Locate and identify every blood parasite.
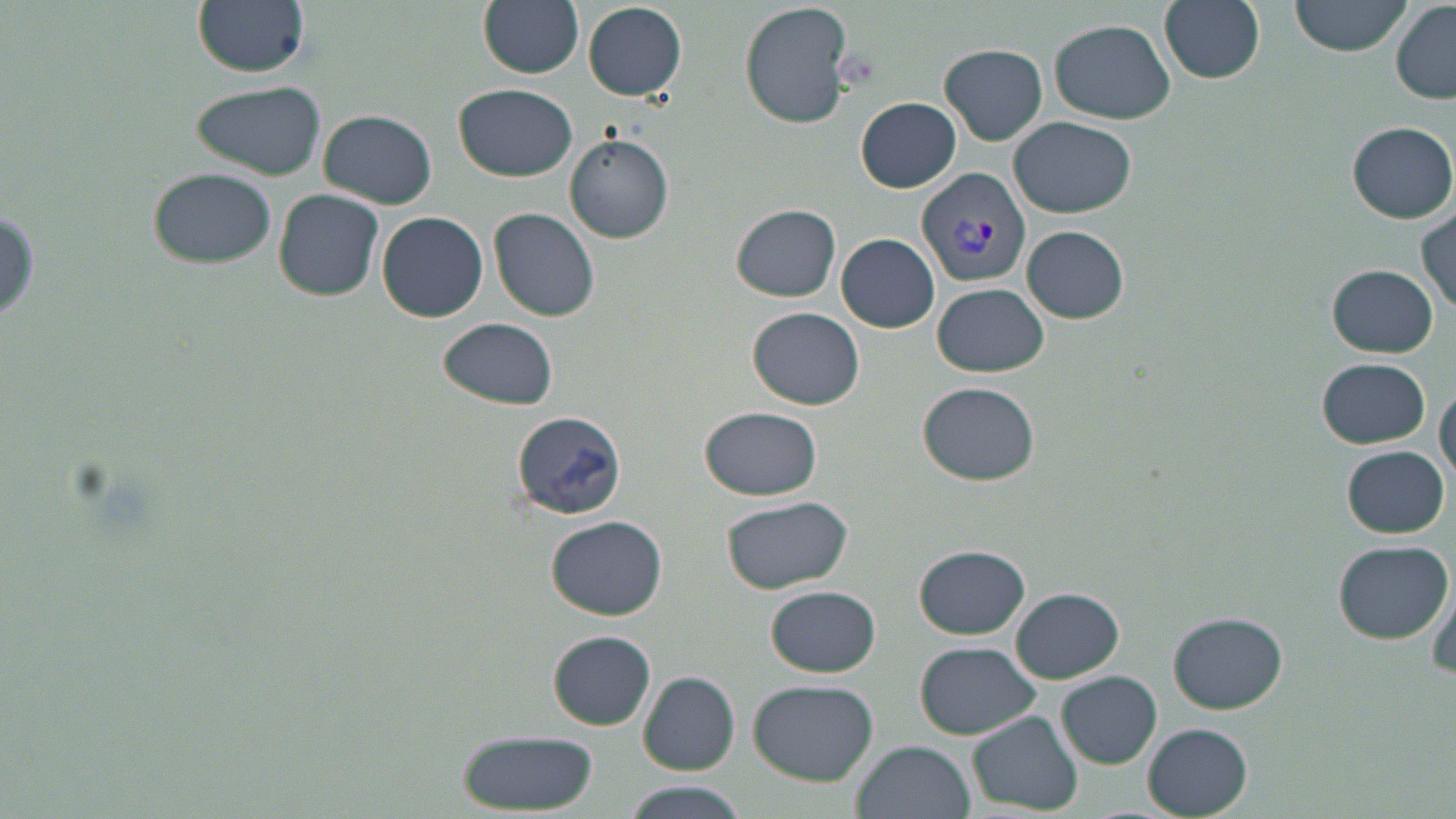

Approximate bounding boxes as (x1, y1, x2, y2) in pixels.
Plasmodium vivax-infected red blood cells: (916, 167, 1031, 290).
No Plasmodium falciparum, Plasmodium ovale, Plasmodium malariae, Babesia divergens, or Trypanosoma brucei observed.

Summary:
  - Uninfected red blood cell locations: (194, 0, 311, 77), (480, 0, 585, 77), (739, 0, 856, 131), (1158, 0, 1266, 85), (1290, 0, 1414, 56), (1392, 2, 1456, 103), (583, 3, 686, 100), (1049, 18, 1175, 123), (941, 43, 1049, 144), (189, 79, 327, 182), (454, 82, 578, 182), (857, 97, 960, 193), (317, 109, 437, 208), (1010, 115, 1136, 218), (1350, 121, 1455, 222), (564, 135, 674, 242), (149, 167, 276, 269), (274, 188, 384, 300), (731, 204, 841, 302), (1416, 205, 1455, 311), (489, 208, 601, 320), (377, 211, 488, 322), (1022, 226, 1128, 322), (837, 233, 939, 332), (1329, 265, 1439, 356), (932, 282, 1049, 378), (748, 307, 865, 410), (438, 316, 559, 411), (1316, 356, 1431, 448), (919, 381, 1038, 486), (1436, 382, 1456, 486), (700, 405, 824, 501), (511, 411, 627, 519), (1344, 446, 1449, 536), (720, 495, 853, 595), (549, 516, 667, 619), (1331, 539, 1454, 642), (913, 545, 1029, 640), (1425, 576, 1456, 683), (766, 585, 881, 677), (1012, 588, 1122, 682), (1168, 614, 1286, 714), (548, 631, 656, 730), (915, 641, 1041, 739), (638, 671, 739, 774), (1058, 671, 1162, 768), (748, 679, 878, 784), (967, 711, 1081, 813), (1141, 723, 1253, 816), (453, 730, 600, 814), (850, 741, 975, 819), (621, 784, 746, 819)
  - Slide-level diagnosis: Plasmodium vivax
  - Field of view: single
  - Preparation: thin blood smear
  - Magnification: 1000x
  - Modality: optical microscopy
  - Image size: 1456×819 pixels
  - Stain: May-Grünwald-Giemsa